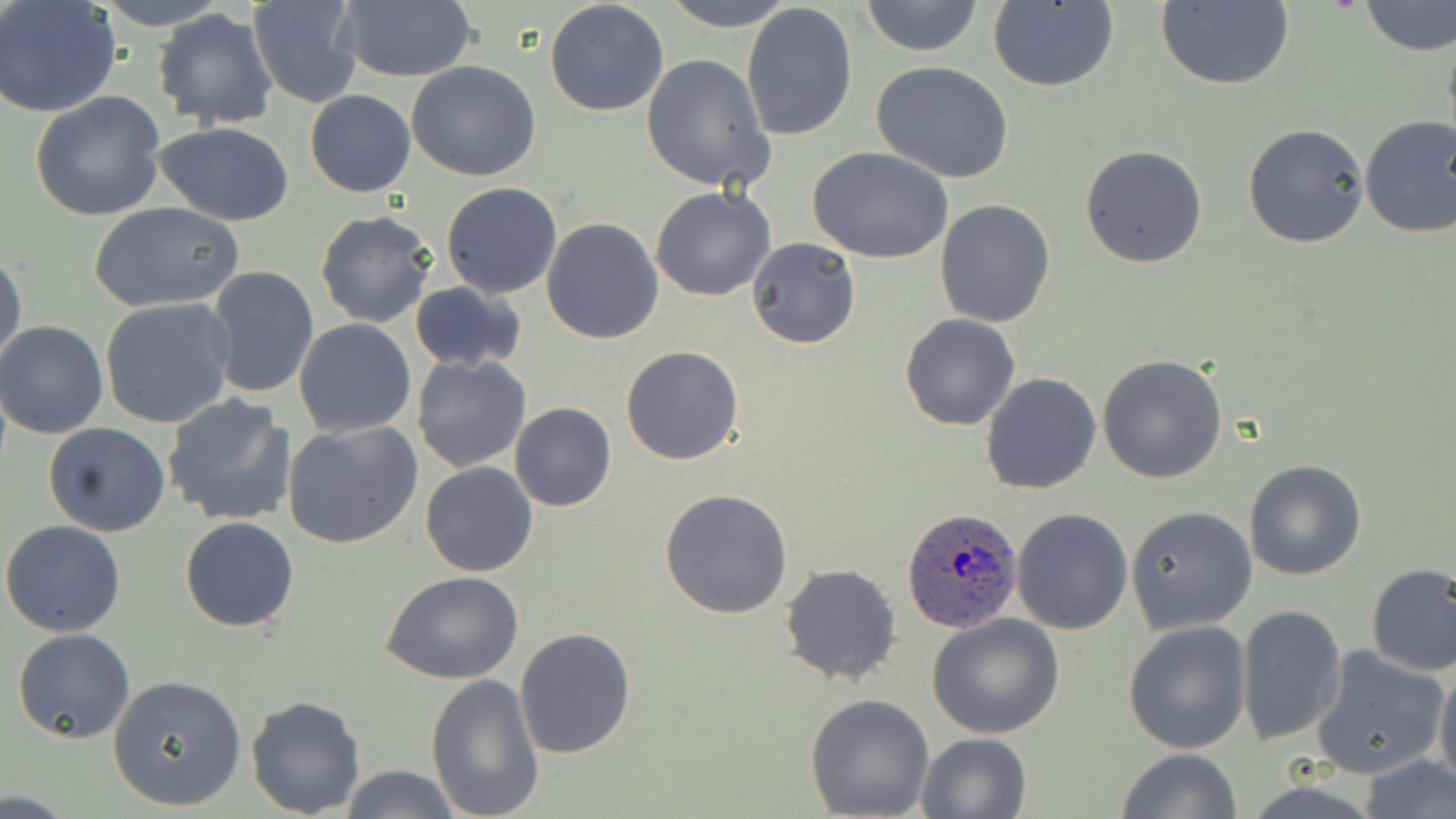
Approximate bounding boxes as [x1, y1, x2, y2] in pixels. Uninfected red blood cell locations: [90, 0, 232, 31], [246, 0, 364, 108], [335, 0, 481, 84], [662, 0, 794, 30], [860, 0, 983, 57], [0, 1, 122, 119], [543, 1, 670, 117], [1155, 1, 1295, 90], [1360, 1, 1456, 55], [740, 2, 857, 143], [987, 2, 1118, 92], [151, 9, 280, 131], [1442, 25, 1456, 154], [641, 53, 773, 191], [407, 60, 542, 182], [871, 61, 1016, 184], [305, 90, 415, 198], [28, 91, 168, 223], [1357, 116, 1456, 240], [153, 122, 297, 227], [1242, 123, 1370, 249], [1080, 144, 1208, 267], [809, 147, 955, 262], [441, 181, 563, 299], [649, 185, 777, 302], [934, 200, 1056, 327], [89, 203, 242, 313], [314, 209, 439, 328], [541, 218, 664, 345], [747, 238, 861, 350], [0, 246, 27, 376], [206, 266, 319, 399], [408, 281, 527, 373], [99, 298, 238, 430], [898, 312, 1021, 432], [294, 319, 416, 438], [0, 321, 109, 438], [621, 345, 744, 465], [411, 353, 532, 474], [1097, 353, 1227, 483], [980, 372, 1103, 495], [163, 394, 297, 526], [509, 403, 617, 512], [282, 421, 423, 550], [42, 422, 170, 537], [1243, 459, 1367, 581], [421, 462, 538, 578], [659, 488, 794, 618], [1126, 506, 1258, 634], [1012, 508, 1133, 635], [180, 516, 299, 633], [1, 520, 127, 636], [779, 563, 903, 687], [1366, 563, 1456, 677], [381, 571, 525, 684], [1236, 604, 1348, 746], [928, 614, 1064, 739], [1122, 621, 1254, 755], [515, 627, 635, 759], [12, 628, 135, 744], [1310, 646, 1448, 780], [1434, 664, 1456, 794], [106, 675, 247, 812], [425, 675, 544, 819], [244, 694, 366, 816], [804, 694, 934, 817], [917, 734, 1034, 819], [1116, 749, 1241, 819], [1354, 756, 1456, 819], [338, 765, 462, 819]. Plasmodium ovale-infected red blood cell locations: [903, 507, 1024, 633]. Slide-level diagnosis: Plasmodium ovale. May-Grünwald-Giemsa stain. Optical microscopy. Thin blood film. Image is 1456×819 pixels. One field of a larger specimen. Captured at 1000x magnification.